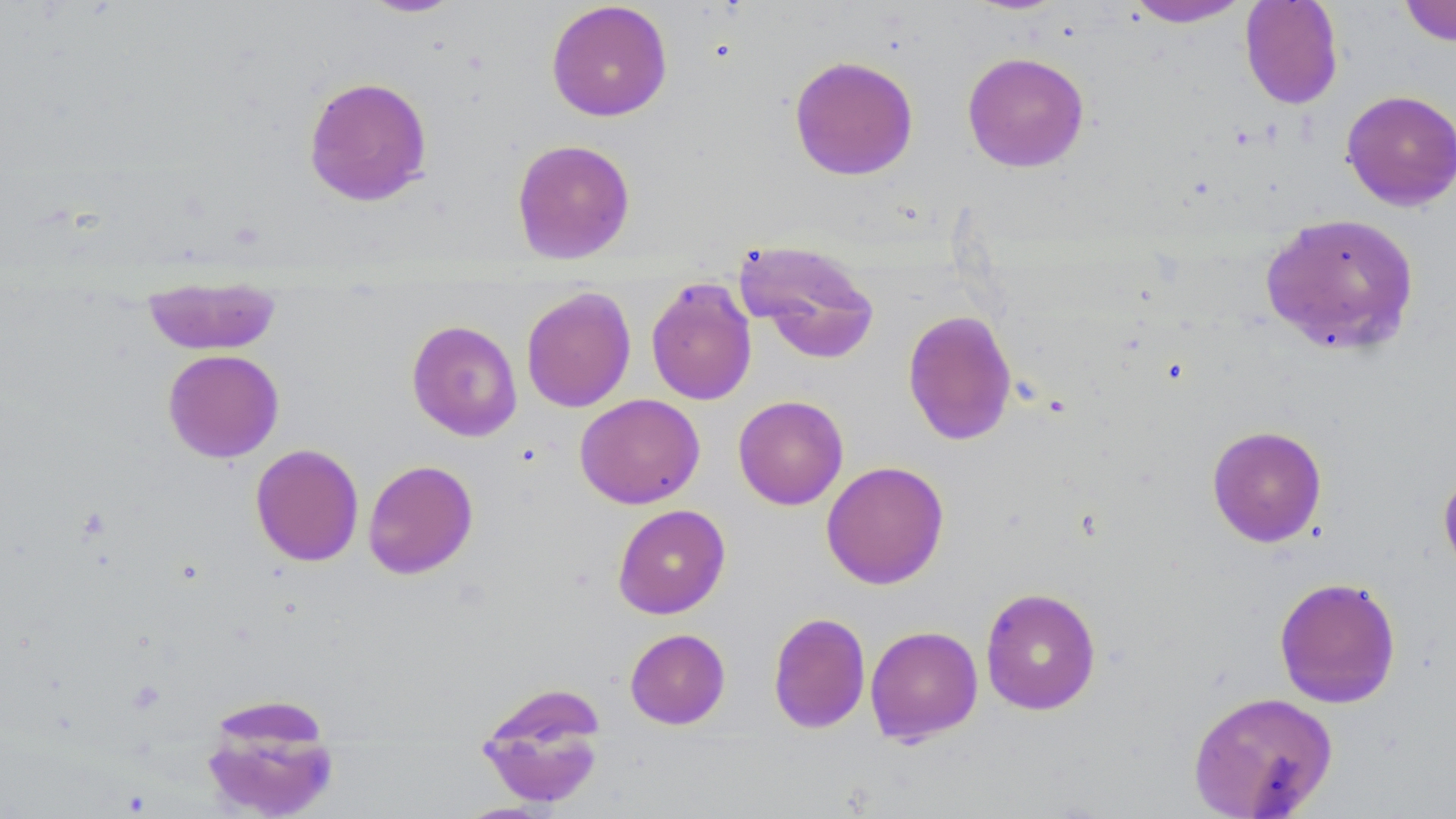
Summary:
  - Coordinate format: approximate bounding boxes as named x1/y1/x2/y2 corners in pixels
  - Uninfected red blood cell locations: (x1=357, y1=0, x2=467, y2=19), (x1=1123, y1=0, x2=1252, y2=27), (x1=1240, y1=0, x2=1344, y2=109), (x1=546, y1=1, x2=673, y2=122), (x1=1397, y1=1, x2=1456, y2=47), (x1=962, y1=51, x2=1090, y2=173), (x1=788, y1=55, x2=919, y2=181), (x1=303, y1=76, x2=433, y2=206), (x1=1341, y1=89, x2=1456, y2=211), (x1=511, y1=139, x2=636, y2=264), (x1=1259, y1=211, x2=1421, y2=356), (x1=735, y1=238, x2=881, y2=365), (x1=142, y1=274, x2=282, y2=356), (x1=645, y1=277, x2=757, y2=406), (x1=521, y1=286, x2=636, y2=412), (x1=902, y1=309, x2=1017, y2=446), (x1=406, y1=320, x2=523, y2=442), (x1=162, y1=349, x2=284, y2=462), (x1=574, y1=393, x2=705, y2=509), (x1=733, y1=395, x2=848, y2=510), (x1=1207, y1=425, x2=1327, y2=547), (x1=250, y1=443, x2=364, y2=567), (x1=362, y1=460, x2=479, y2=580), (x1=821, y1=460, x2=949, y2=590), (x1=1438, y1=465, x2=1456, y2=581), (x1=612, y1=504, x2=730, y2=619), (x1=1274, y1=576, x2=1402, y2=708), (x1=980, y1=587, x2=1102, y2=715), (x1=768, y1=612, x2=871, y2=734), (x1=864, y1=625, x2=983, y2=745), (x1=624, y1=628, x2=730, y2=729), (x1=475, y1=683, x2=608, y2=810), (x1=1187, y1=690, x2=1338, y2=818), (x1=199, y1=697, x2=341, y2=819)
  - Slide-level diagnosis: negative for blood parasites
  - Modality: light microscopy
  - Magnification: 1000x
  - Stain: May-Grünwald-Giemsa
  - Field of view: single
  - Image size: 1456×819 pixels
  - Preparation: thin blood film